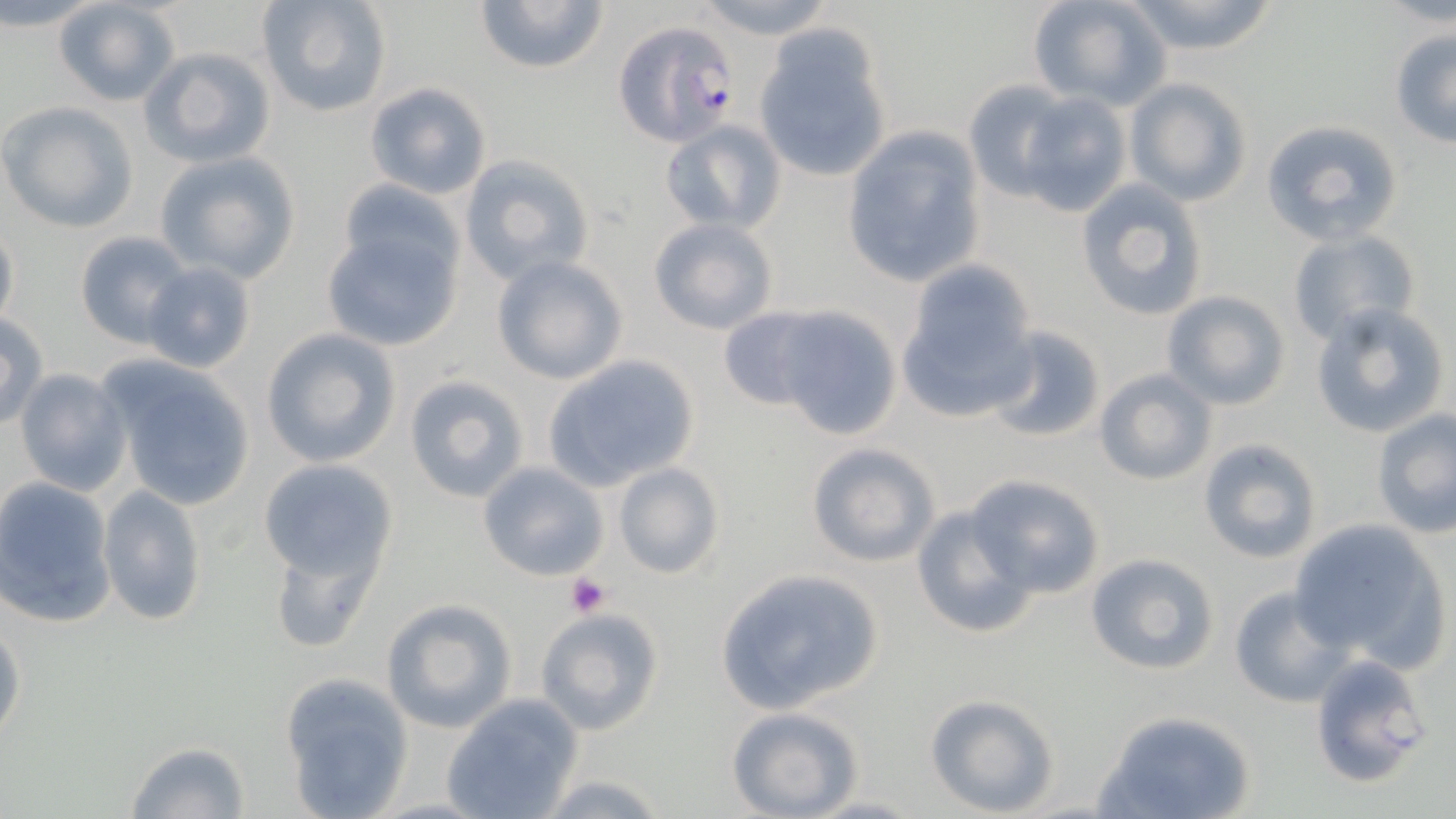
{
  "slide_level_diagnosis": "Plasmodium falciparum",
  "image_size": "1456×819 pixels",
  "magnification": "1000x",
  "plasmodium_falciparum_infected_red_blood_cell_locations": "approximate bounding boxes as [x1, y1, x2, y2] in pixels: [614, 19, 741, 148]",
  "uninfected_red_blood_cell_locations": "approximate bounding boxes as [x1, y1, x2, y2] in pixels: [51, 0, 181, 106], [256, 0, 393, 119], [474, 0, 609, 73], [689, 0, 841, 42], [1028, 0, 1173, 112], [1119, 0, 1281, 57], [754, 24, 892, 184], [1389, 29, 1456, 149], [141, 47, 276, 169], [1126, 78, 1251, 206], [963, 79, 1080, 198], [364, 82, 492, 201], [1011, 88, 1134, 217], [0, 102, 139, 232], [660, 119, 787, 236], [1259, 119, 1403, 246], [839, 126, 988, 289], [153, 152, 302, 283], [460, 155, 594, 286], [1076, 180, 1207, 322], [332, 183, 467, 297], [648, 217, 779, 335], [319, 221, 463, 352], [0, 222, 20, 334], [1285, 228, 1419, 346], [76, 232, 194, 346], [490, 255, 626, 385], [142, 261, 257, 374], [898, 272, 1037, 419], [1160, 289, 1290, 410], [1308, 301, 1449, 439], [717, 306, 834, 411], [771, 306, 905, 437], [0, 311, 49, 433], [983, 325, 1108, 445], [261, 327, 402, 468], [544, 353, 701, 490], [101, 360, 257, 511], [12, 367, 132, 497], [1093, 368, 1216, 488], [403, 373, 531, 503], [1370, 409, 1456, 536], [1198, 439, 1322, 564], [805, 442, 940, 568], [257, 460, 397, 587], [477, 461, 609, 581], [612, 461, 724, 579], [969, 474, 1103, 599], [0, 476, 118, 628], [98, 484, 207, 627], [909, 502, 1036, 640], [1289, 519, 1448, 669], [267, 537, 383, 654], [1086, 552, 1218, 676], [714, 567, 885, 714], [1230, 586, 1350, 707], [381, 600, 516, 733], [535, 606, 665, 736], [0, 621, 25, 746], [1309, 654, 1434, 789], [282, 673, 415, 818], [922, 692, 1062, 817], [441, 694, 584, 819], [725, 706, 864, 819], [1095, 710, 1258, 819], [124, 742, 255, 819], [535, 774, 673, 817], [804, 794, 926, 817]",
  "stain": "May-Grünwald-Giemsa",
  "platelet_locations": "approximate bounding boxes as [x1, y1, x2, y2] in pixels: [565, 573, 609, 617]",
  "field_of_view": "one of a larger specimen",
  "modality": "optical microscopy",
  "preparation": "thin blood film"
}